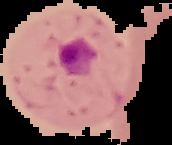

image size = 172×145 pixels
preparation = thin blood smear
result = malaria parasites detected
image type = segmented cell region on a black background